Report the malaria status of this cell.
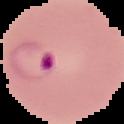

Parasitized.

Summary:
  - Image size: 124×124 pixels
  - Preparation: thin blood smear
  - Image type: segmented cell region with the area outside set to black